State which parasite is depicted.
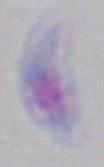

Toxoplasma gondii.

Captured at 1000x magnification. Micrograph.